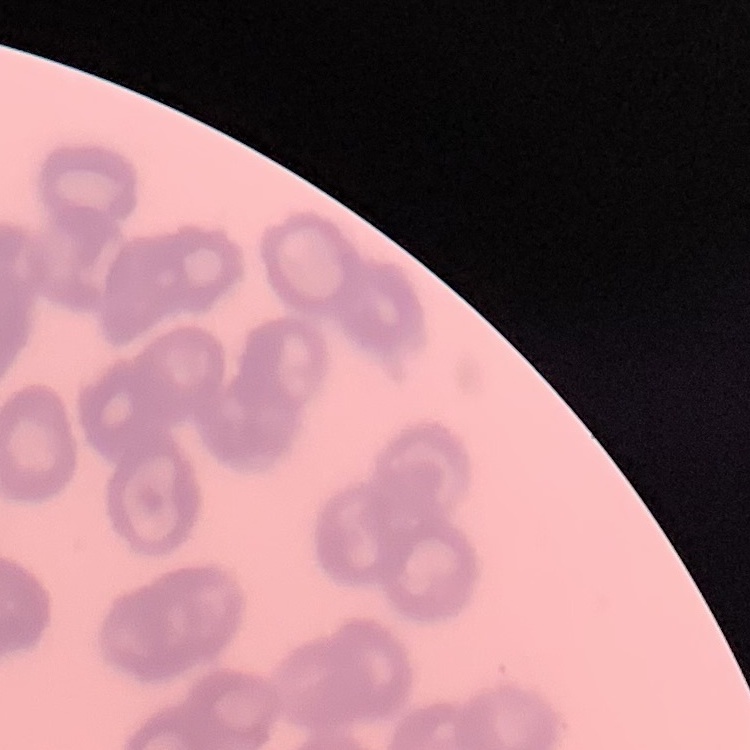
Summary:
  - Red blood cell morphology: rouleaux formation
  - Stain: Field's or Giemsa
  - Preparation: thin peripheral smear
  - Image type: square crop of a larger photomicrograph